Classify this cell by malaria status.
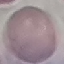
Uninfected.

stain: Giemsa
capture: smartphone through the microscope eyepiece
preparation: thin blood film
image_type: automatically extracted cell patch, resized to 64 × 64 pixels